Name the blood parasite species.
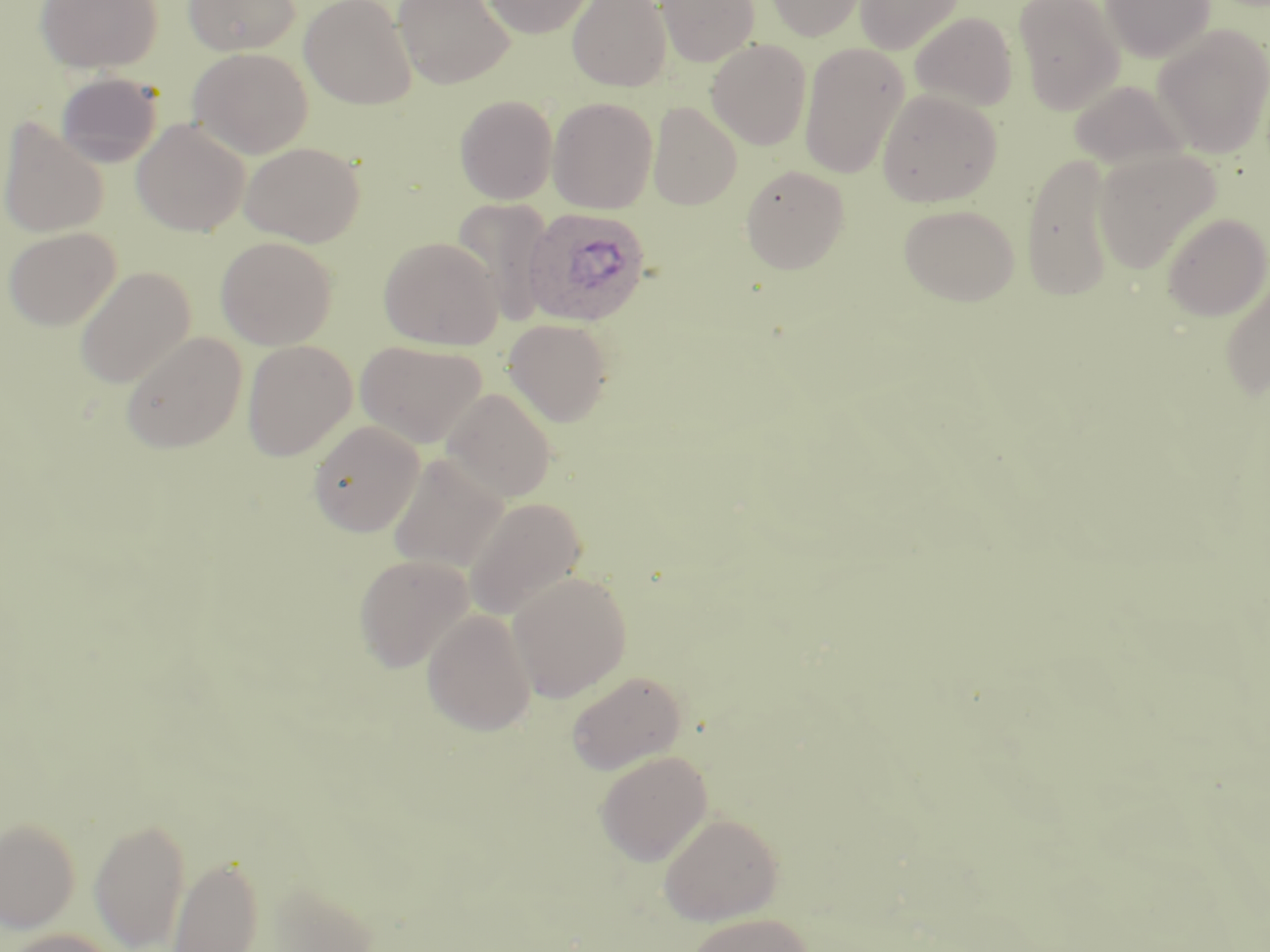
Plasmodium ovale.

Summary:
  - Coordinate format: approximate bounding boxes as [x1, y1, x2, y2] in pixels
  - Uninfected red blood cell locations: [35, 0, 163, 74], [184, 0, 300, 55], [299, 0, 417, 109], [393, 0, 515, 89], [480, 0, 595, 38], [567, 0, 671, 91], [656, 0, 760, 66], [765, 0, 868, 41], [855, 0, 965, 55], [1013, 0, 1125, 115], [1100, 0, 1216, 63], [909, 11, 1018, 112], [1152, 24, 1270, 158], [706, 39, 812, 150], [799, 42, 909, 180], [188, 47, 313, 159], [56, 72, 163, 168], [1068, 78, 1191, 171], [877, 89, 1002, 207], [454, 94, 558, 204], [548, 97, 658, 213], [648, 102, 742, 209], [131, 118, 250, 236], [0, 119, 109, 239], [240, 141, 365, 246], [1093, 149, 1221, 273], [1020, 152, 1118, 301], [740, 164, 850, 274], [450, 197, 554, 326], [898, 203, 1020, 305], [1161, 212, 1269, 321], [3, 227, 121, 331], [215, 236, 338, 350], [379, 236, 502, 350], [75, 266, 195, 389], [1219, 274, 1270, 400], [503, 319, 614, 426], [120, 331, 248, 454], [241, 340, 357, 461], [356, 340, 487, 449], [443, 388, 557, 503], [307, 420, 424, 537], [388, 452, 509, 574], [465, 496, 588, 621], [353, 554, 476, 672], [507, 571, 632, 701], [421, 609, 536, 736], [565, 670, 687, 775], [595, 750, 712, 865], [658, 812, 783, 925], [89, 816, 191, 952], [0, 817, 81, 933], [168, 854, 264, 952], [255, 878, 382, 951], [686, 912, 813, 952], [3, 928, 121, 952]
  - Plasmodium ovale-infected red blood cell locations: [522, 206, 651, 327]
  - Image size: 1270×952 pixels
  - Stain: May-Grünwald-Giemsa
  - Field of view: one of a larger specimen
  - Preparation: thin blood smear
  - Magnification: 1000x
  - Modality: optical microscopy